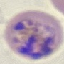
Summary:
  - Result: malaria parasites identified
  - Capture: smartphone through the microscope eyepiece
  - Preparation: thin blood film
  - Stain: Giemsa
  - Image type: cell patch, automatically extracted from a larger field of view and resized to 64 × 64 pixels